Classify this cell by malaria status.
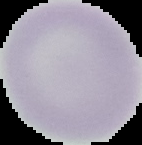

It is uninfected.

Cell region segmented out of the field of view; the surrounding area is masked to black. Image is 142×145 pixels. From a thin blood film.